Locate every blood parasite and identify its species.
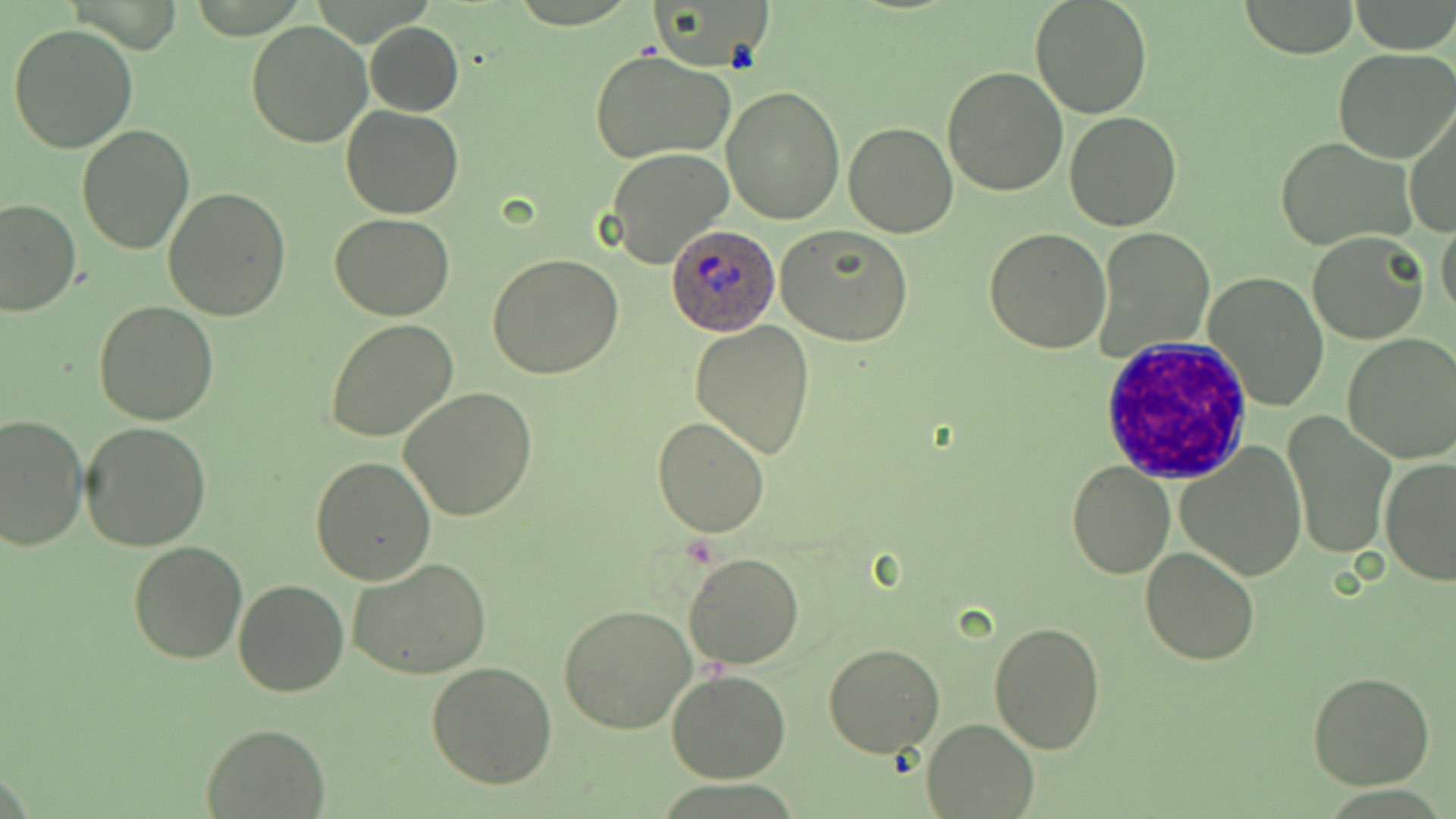
Approximate bounding boxes as named x1/y1/x2/y2 corners in pixels.
Plasmodium ovale-infected red blood cells: (x1=667, y1=222, x2=780, y2=336).
No Plasmodium falciparum, Plasmodium malariae, Plasmodium vivax, Babesia divergens, or Trypanosoma brucei observed.

White blood cell locations: (x1=1098, y1=336, x2=1251, y2=483). Uninfected red blood cell locations: (x1=1028, y1=0, x2=1153, y2=119), (x1=655, y1=1, x2=772, y2=70), (x1=1234, y1=1, x2=1360, y2=57), (x1=246, y1=21, x2=372, y2=148), (x1=7, y1=22, x2=139, y2=155), (x1=366, y1=22, x2=463, y2=116), (x1=589, y1=48, x2=735, y2=165), (x1=1334, y1=48, x2=1456, y2=163), (x1=942, y1=66, x2=1070, y2=196), (x1=722, y1=86, x2=844, y2=224), (x1=1405, y1=103, x2=1455, y2=240), (x1=341, y1=105, x2=465, y2=219), (x1=1065, y1=109, x2=1182, y2=230), (x1=843, y1=122, x2=958, y2=238), (x1=76, y1=126, x2=194, y2=254), (x1=1277, y1=139, x2=1416, y2=249), (x1=605, y1=146, x2=733, y2=269), (x1=163, y1=187, x2=292, y2=320), (x1=0, y1=197, x2=79, y2=317), (x1=331, y1=214, x2=455, y2=322), (x1=1437, y1=217, x2=1456, y2=324), (x1=777, y1=226, x2=916, y2=348), (x1=983, y1=228, x2=1111, y2=354), (x1=1096, y1=228, x2=1213, y2=360), (x1=1308, y1=230, x2=1430, y2=344), (x1=489, y1=252, x2=624, y2=377), (x1=1203, y1=272, x2=1330, y2=410), (x1=93, y1=301, x2=218, y2=425), (x1=325, y1=319, x2=459, y2=442), (x1=690, y1=319, x2=816, y2=459), (x1=1340, y1=333, x2=1456, y2=463), (x1=398, y1=386, x2=537, y2=522), (x1=0, y1=412, x2=88, y2=551), (x1=1283, y1=412, x2=1396, y2=560), (x1=652, y1=415, x2=773, y2=537), (x1=79, y1=421, x2=213, y2=553), (x1=1176, y1=439, x2=1308, y2=580), (x1=310, y1=456, x2=437, y2=587), (x1=1380, y1=457, x2=1456, y2=586), (x1=1066, y1=460, x2=1175, y2=581), (x1=127, y1=540, x2=248, y2=664), (x1=1138, y1=546, x2=1260, y2=666), (x1=684, y1=553, x2=804, y2=670), (x1=348, y1=559, x2=493, y2=678), (x1=232, y1=579, x2=348, y2=697), (x1=558, y1=604, x2=700, y2=735), (x1=987, y1=622, x2=1107, y2=753), (x1=824, y1=642, x2=945, y2=757), (x1=427, y1=661, x2=558, y2=788), (x1=666, y1=671, x2=791, y2=783), (x1=1307, y1=671, x2=1435, y2=790), (x1=921, y1=718, x2=1038, y2=818), (x1=200, y1=723, x2=329, y2=817). Slide-level diagnosis: Plasmodium ovale. Thin blood film. Single field of view. Image is 1456×819 pixels. Captured at 1000x magnification. May-Grünwald-Giemsa-stained preparation. Light microscopy.